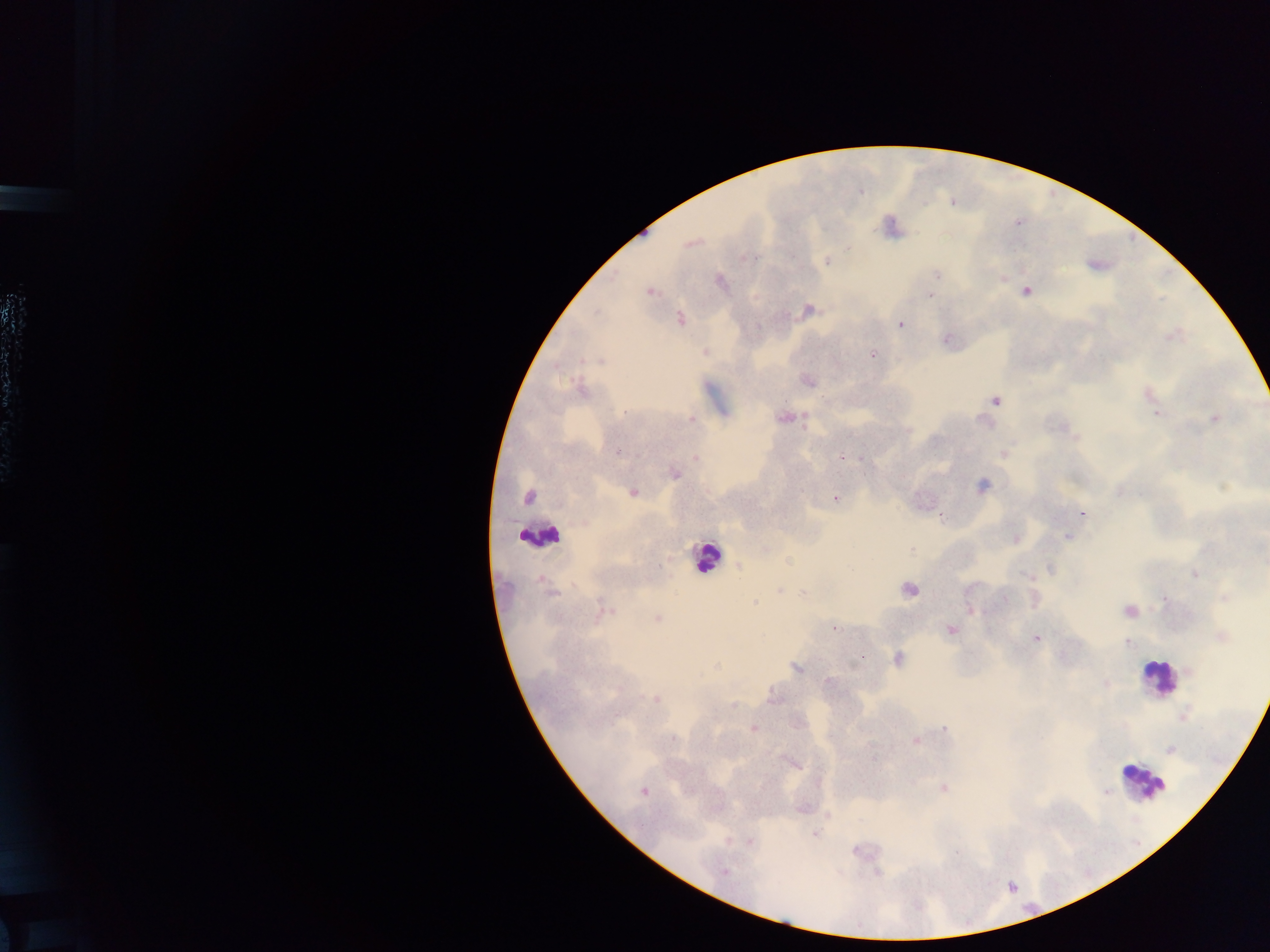

Approximate centers as (x, y) in pixels.
Summary:
  - Leukocyte locations: (539, 534), (706, 556), (1157, 677), (1144, 782)
  - Plasmodium parasite locations: (952, 202), (1017, 223), (691, 244), (848, 247), (748, 257), (827, 262), (937, 274), (1003, 279), (720, 281), (649, 292), (1026, 292), (929, 295), (808, 310), (597, 313), (680, 319), (901, 325), (946, 340), (705, 352), (873, 355), (601, 361), (807, 381), (582, 389), (1148, 394), (996, 400), (626, 412), (1157, 413), (784, 418), (691, 419), (1214, 419), (618, 452), (1004, 453), (842, 457), (696, 458), (862, 458), (674, 475), (982, 485), (633, 492), (527, 496), (835, 498), (1081, 513), (942, 517), (1067, 536), (1016, 539), (912, 549), (789, 562), (739, 567), (1051, 569), (1195, 574), (1026, 575), (908, 589), (780, 590), (550, 593), (803, 594), (1225, 597), (1164, 599), (1005, 600), (754, 603), (604, 611), (973, 611), (1129, 611), (657, 619), (834, 628), (950, 630), (1222, 637), (1036, 639), (1127, 643), (898, 659), (716, 666), (796, 668), (828, 682), (1106, 683), (773, 697), (655, 699), (733, 705), (1184, 716), (945, 728), (753, 729), (673, 738), (915, 740), (1171, 750), (795, 763), (943, 788), (1105, 791), (643, 792), (814, 833), (749, 841), (725, 872)
  - Preparation: thick blood film
  - Image size: 1270×952 pixels
  - Capture: mobile-phone photograph through a microscope
  - Field of view: single
  - Country: Ghana